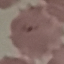
Malaria status: parasitized. Thin blood smear. Automatically extracted cell patch, resized to 64 × 64 pixels. Giemsa stain. Acquired by smartphone through the microscope eyepiece.